State the preparation type.
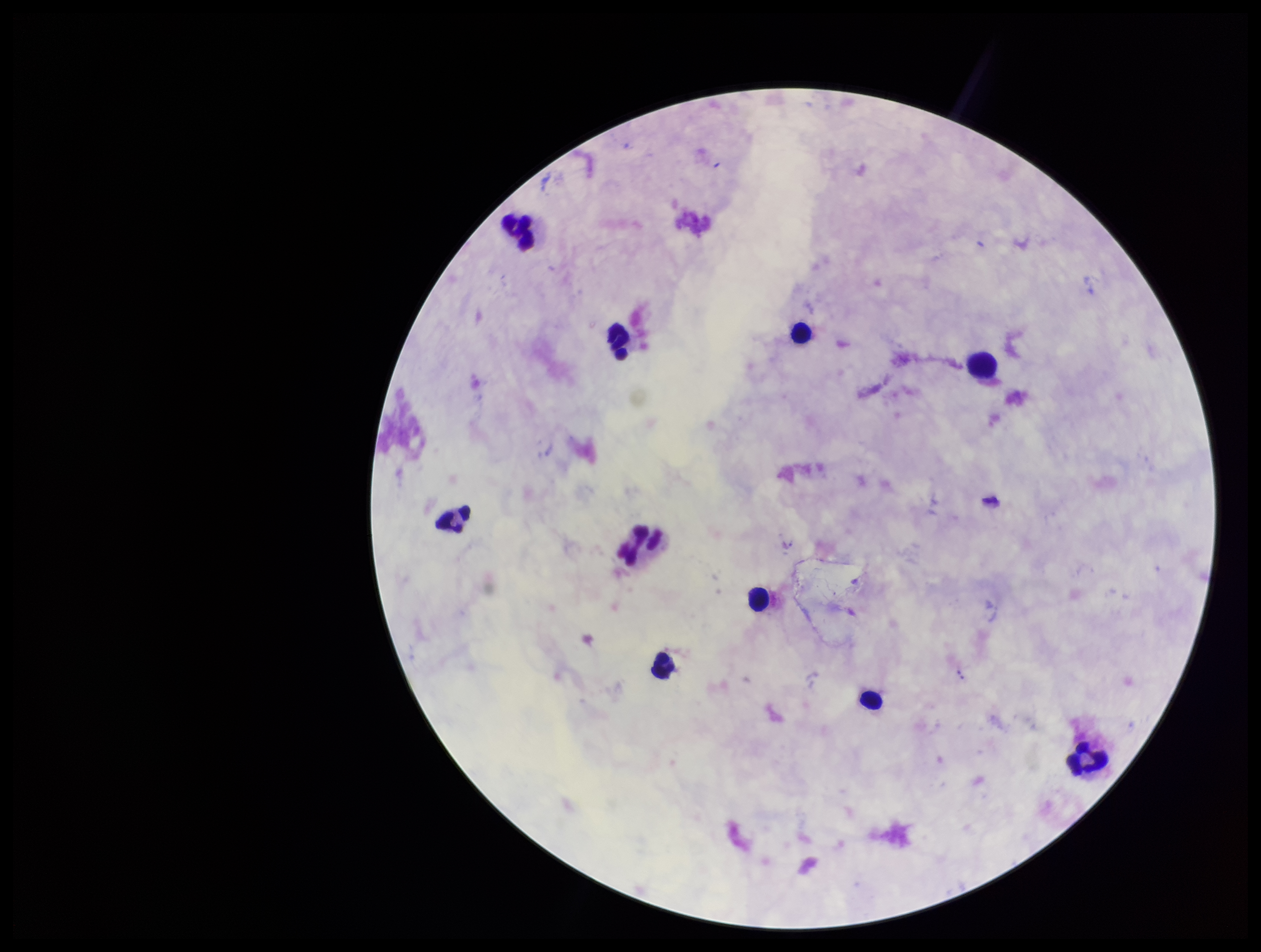

It is a thick blood smear.

One field from this slide. Plasmodium parasites: none detected. Parasite count: 0. Patient malaria status: negative. Leukocyte count: 10. Smartphone photograph taken through the eyepiece of a microscope. Giemsa stain. Image is 1261×952 pixels.